Point out every Plasmodium parasite and every leukocyte.
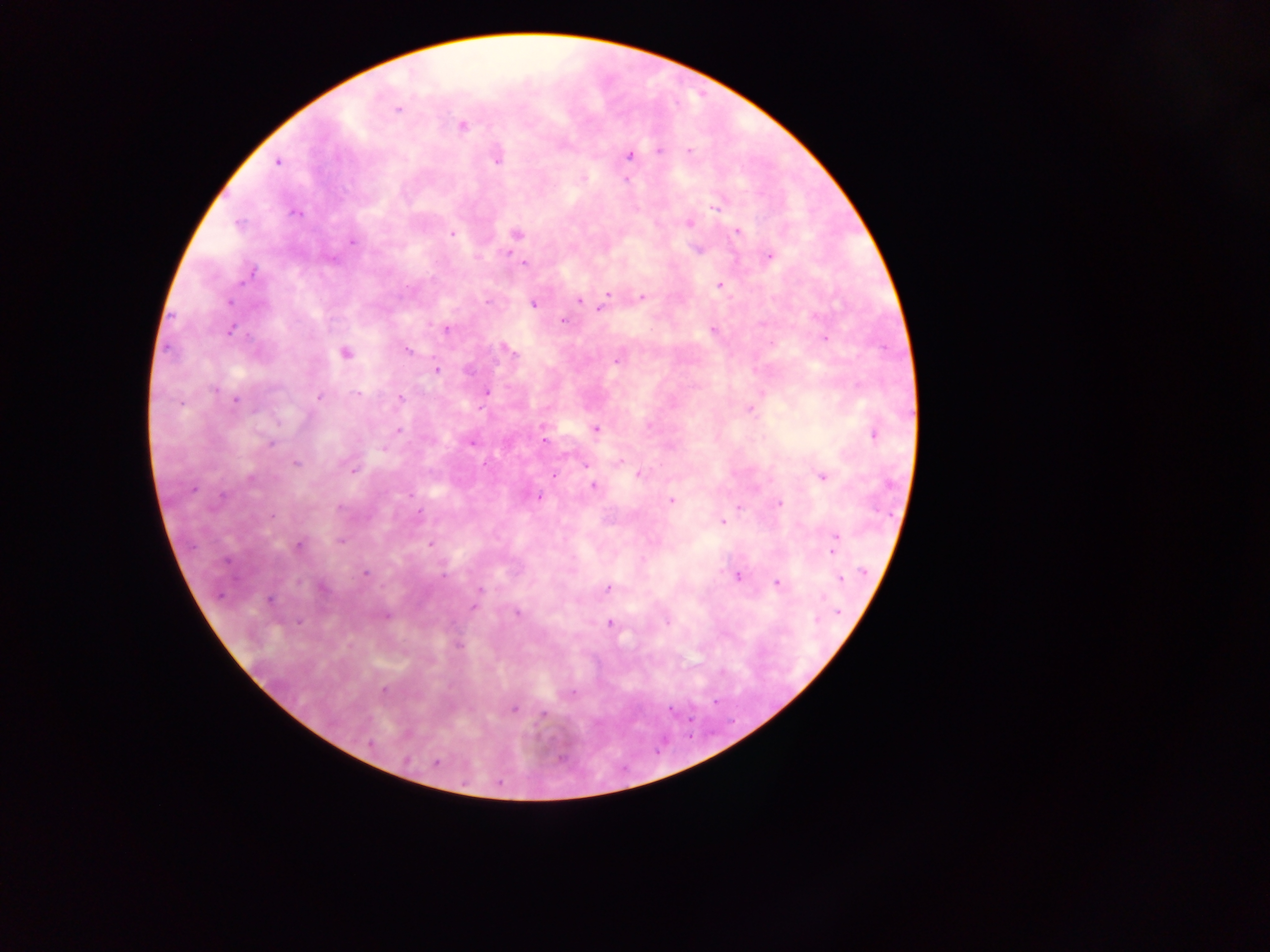
Approximate centers as [x, y] in pixels.
Plasmodium parasites: [397, 110], [463, 127], [659, 151], [689, 151], [629, 155], [496, 160], [277, 162], [626, 180], [716, 207], [295, 212], [688, 223], [238, 225], [737, 231], [452, 234], [516, 234], [352, 242], [697, 249], [770, 256], [524, 263], [252, 272], [719, 285], [608, 295], [641, 297], [579, 300], [228, 302], [487, 302], [533, 303], [601, 308], [563, 320], [447, 329], [712, 330], [231, 331], [825, 339], [510, 349], [408, 350], [346, 353], [618, 359], [436, 370], [214, 389], [486, 391], [357, 394], [319, 398], [400, 398], [236, 400], [749, 409], [648, 425], [595, 429], [399, 431], [874, 435], [543, 441], [471, 443], [271, 444], [296, 463], [586, 465], [352, 471], [639, 474], [554, 475], [823, 477], [250, 479], [593, 485], [192, 489], [409, 495], [223, 496], [540, 497], [671, 501], [780, 503], [340, 507], [739, 507], [419, 512], [271, 516], [723, 522], [835, 539], [341, 541], [299, 545], [430, 545], [833, 551], [864, 572], [365, 573], [443, 577], [737, 577], [841, 579], [776, 583], [607, 587], [321, 588], [480, 589], [823, 598], [269, 601], [474, 607], [838, 611], [517, 613], [386, 616], [816, 619], [667, 621], [299, 622], [609, 622], [458, 646], [383, 690], [572, 693], [513, 709], [543, 715], [371, 744], [407, 760], [436, 763].
No leukocytes observed.

image_size: 1270×952 pixels
country: Ghana
field_of_view: single
preparation: thick blood film
capture: mobile-phone photograph through a microscope